Assess the morphology of the erythrocytes.
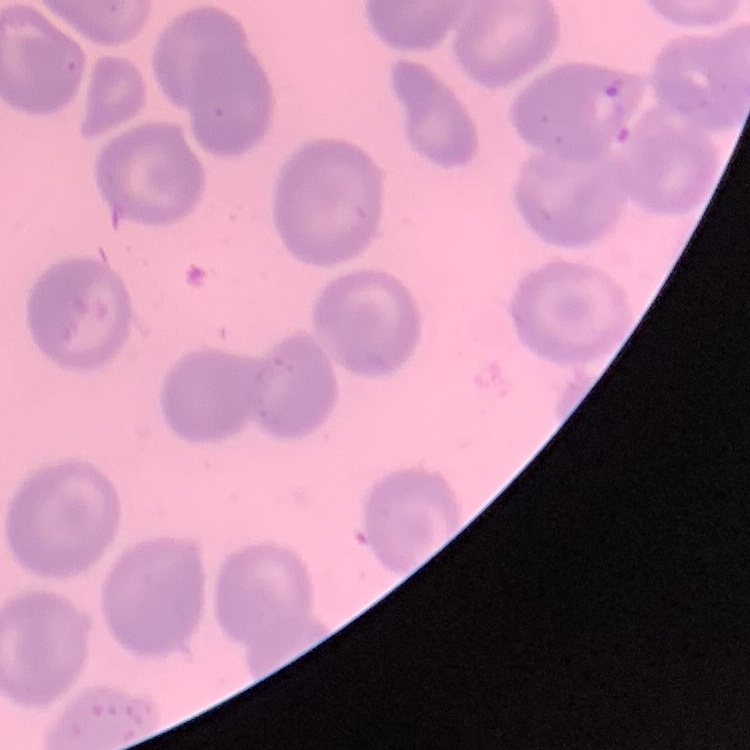
No rouleaux formation.

Summary:
  - Stain: Field's or Giemsa
  - Preparation: thin blood smear
  - Image type: one tile cut from a larger photomicrograph